Assess this cell for malaria.
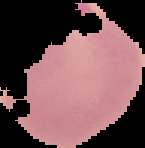
It is parasitized.

preparation: thin blood smear
image_type: cell region segmented out of the field of view; surrounding area masked to black
image_size: 145×148 pixels